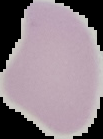
image_size: 103×139 pixels
image_type: segmented cell region with the area outside set to black
preparation: thin blood film
malaria_status: uninfected